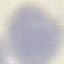

Malaria status: uninfected. Giemsa-stained preparation. Photographed with a smartphone camera at the microscope eyepiece. Thin smear of blood. Cell patch, automatically extracted from a larger field of view and resized to 64 × 64 pixels.